Report the malaria status of this cell.
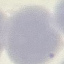

Uninfected.

image_type: automatically extracted cell patch, resized to 64 × 64 pixels
stain: Giemsa
preparation: thin blood film
capture: smartphone camera at the microscope eyepiece